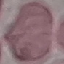
malaria status = uninfected
image type = automatically extracted cell patch, resized to 64 × 64 pixels
preparation = thin blood film
stain = Giemsa
capture = smartphone camera at the microscope eyepiece